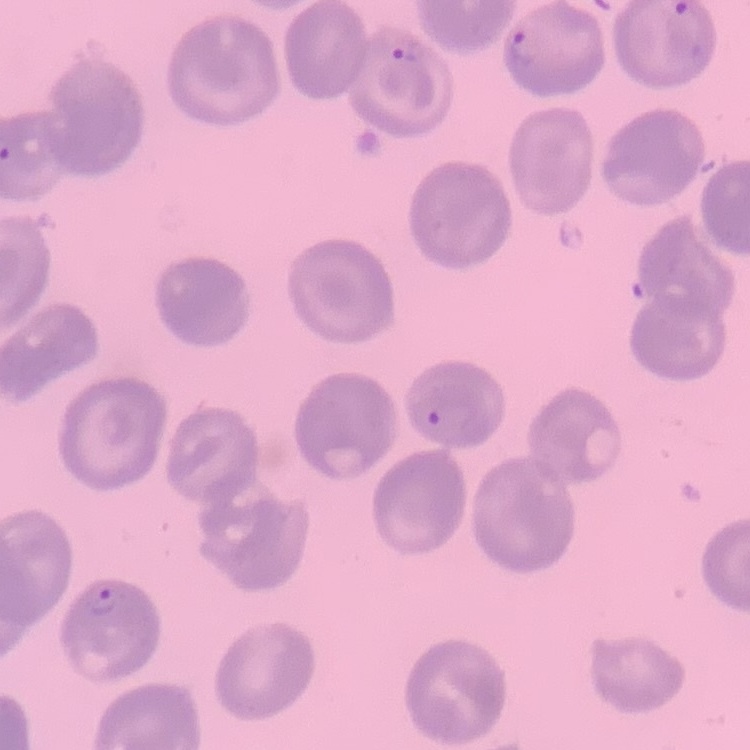 The red blood cells show no rouleaux formation. Field's or Giemsa stain. Square crop of a larger photomicrograph. Thin peripheral smear.